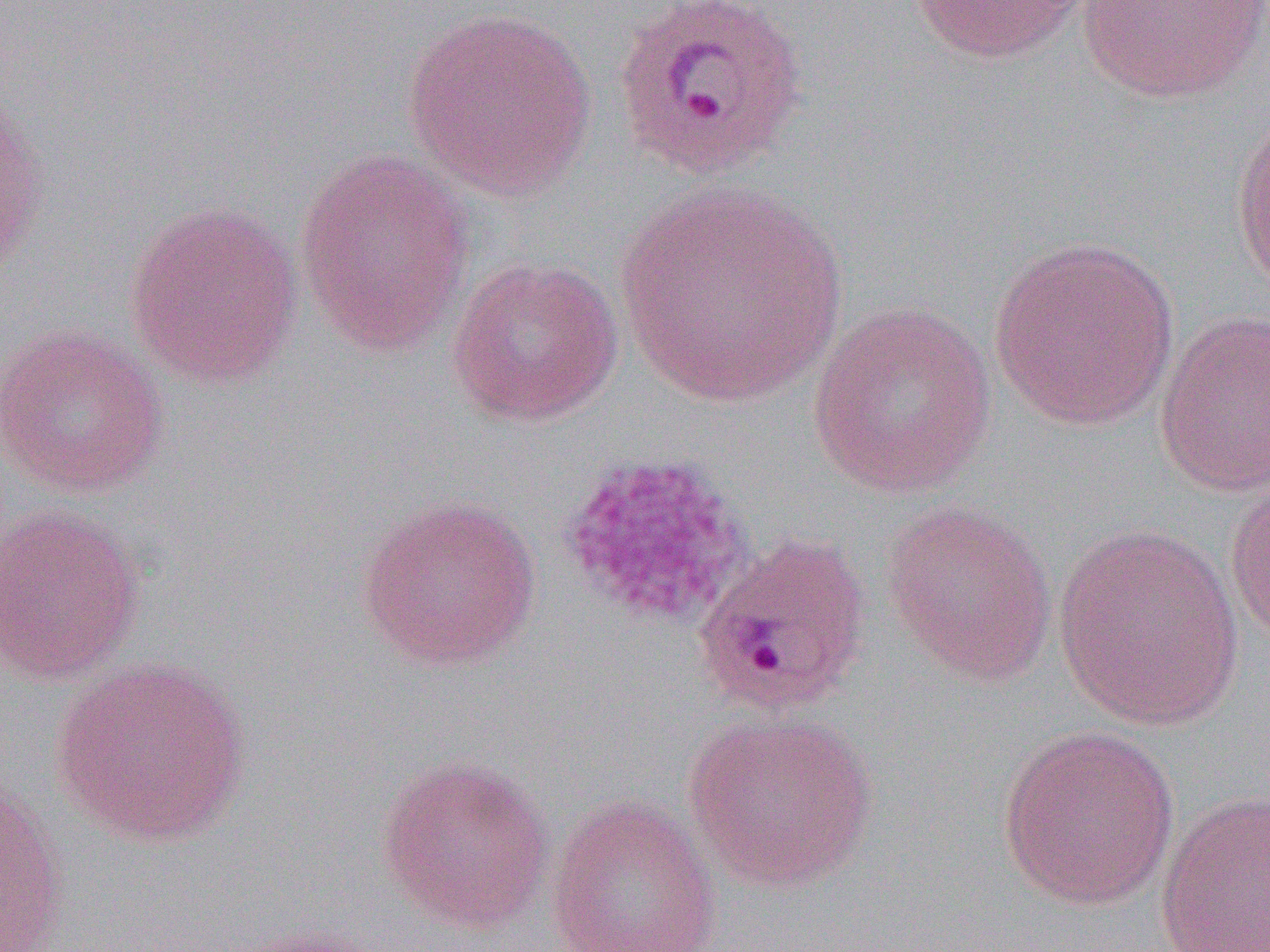

{
  "slide_level_diagnosis": "Plasmodium ovale",
  "uninfected_red_blood_cell_locations": "approximate bounding boxes as [x1, y1, x2, y2] in pixels: [905, 0, 1095, 65], [1076, 1, 1270, 103], [403, 8, 597, 200], [1, 84, 49, 288], [1229, 104, 1270, 298], [294, 148, 474, 356], [615, 184, 846, 408], [123, 200, 304, 388], [988, 235, 1181, 430], [446, 256, 624, 427], [806, 302, 998, 499], [1154, 310, 1270, 498], [0, 324, 171, 498], [1225, 475, 1270, 646], [355, 494, 542, 672], [879, 501, 1058, 686], [0, 503, 145, 686], [1052, 522, 1247, 730], [51, 656, 253, 847], [682, 709, 880, 892], [997, 725, 1180, 911], [375, 754, 556, 934], [0, 778, 67, 952], [1155, 789, 1270, 951], [546, 794, 723, 952], [217, 924, 392, 952]",
  "magnification": "1000x",
  "field_of_view": "single",
  "image_size": "1270×952 pixels",
  "preparation": "thin blood smear",
  "plasmodium_ovale_infected_red_blood_cell_locations": "approximate bounding boxes as [x1, y1, x2, y2] in pixels: [612, 0, 810, 182], [692, 531, 872, 719]",
  "platelet_locations": "approximate bounding boxes as [x1, y1, x2, y2] in pixels: [558, 452, 753, 630]",
  "modality": "light microscopy"
}